Describe the morphology of the red blood cells.
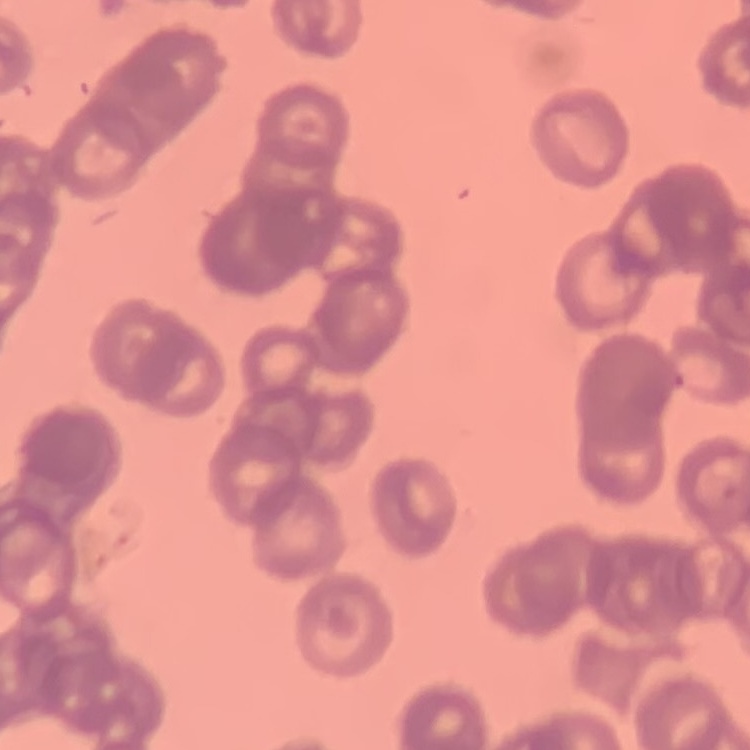

They show rouleaux formation.

Summary:
  - Stain: Field's or Giemsa
  - Image type: square crop of a larger photomicrograph
  - Preparation: thin peripheral smear